Identify the parasite.
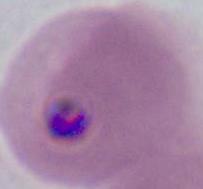
This is Plasmodium.

Summary:
  - Modality: photomicrograph
  - Magnification: 400x or 1000x